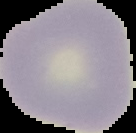

Summary:
  - Image type: cell region segmented out of the field of view; surrounding area masked to black
  - Preparation: thin blood film
  - Result: negative for malaria parasites
  - Image size: 136×133 pixels